State which cell type is depicted.
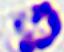
This is a leukocyte.

modality = micrograph
magnification = 400x